Identify the parasite.
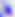
Toxoplasma gondii.

Summary:
  - Magnification: 400x
  - Modality: photomicrograph